Classify this cell by malaria status.
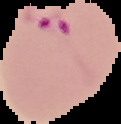
Parasitized.

preparation: thin blood smear
image_size: 121×124 pixels
image_type: segmented cell region on a black background